Locate and identify every blood parasite.
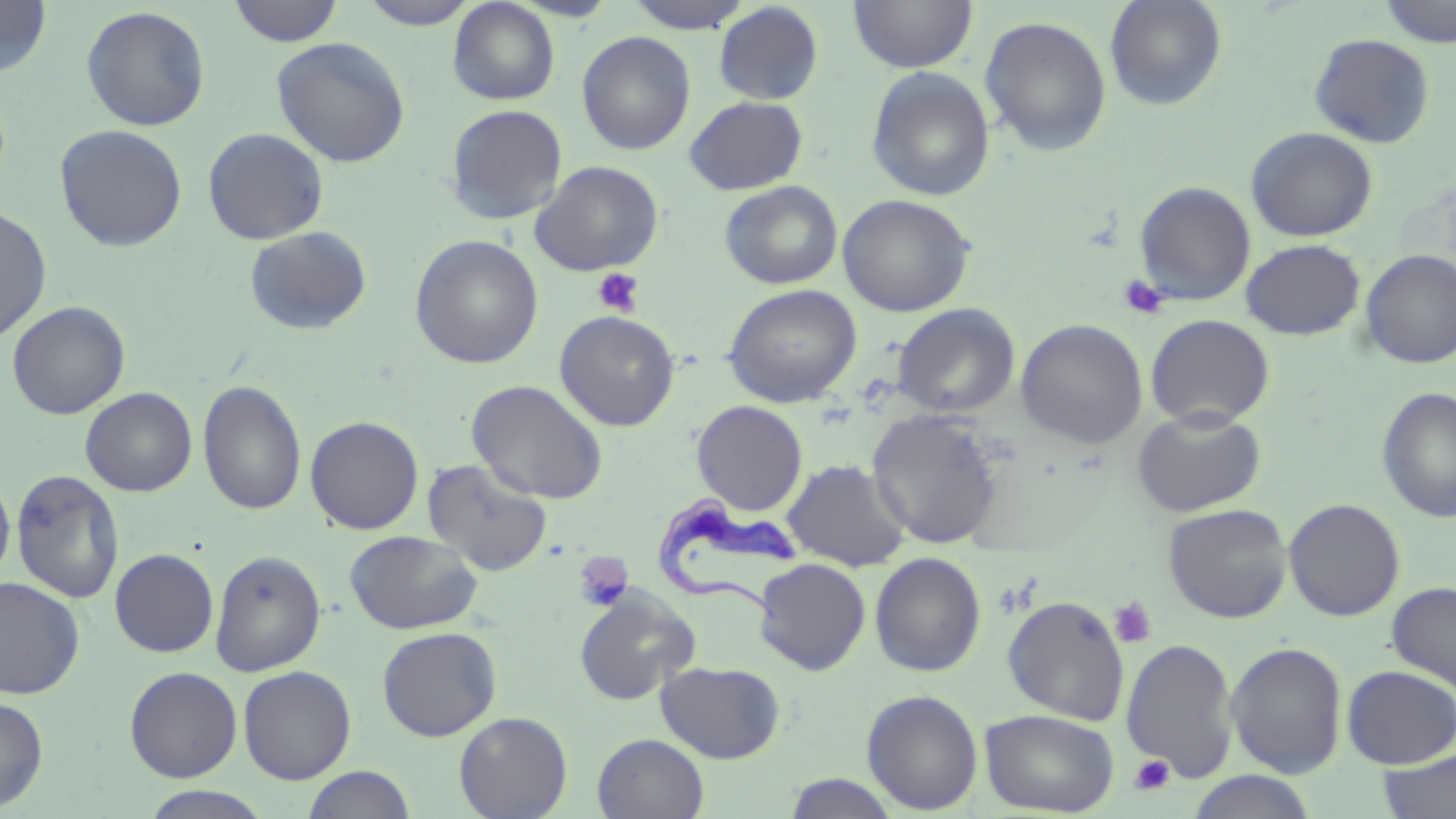
Approximate bounding boxes as (x1, y1, x2, y2) in pixels.
Trypanosoma brucei: (658, 495, 804, 625).
No Plasmodium falciparum, Plasmodium ovale, Plasmodium malariae, Plasmodium vivax, or Babesia divergens observed.

Platelet locations: (591, 267, 645, 317), (1119, 275, 1170, 320), (573, 551, 632, 612), (1109, 597, 1157, 649), (1129, 754, 1175, 796). Uninfected red blood cell locations: (0, 0, 53, 78), (228, 0, 345, 47), (356, 0, 482, 29), (623, 0, 755, 33), (848, 0, 978, 74), (1105, 0, 1228, 111), (1380, 0, 1456, 47), (448, 1, 560, 105), (714, 2, 824, 105), (80, 5, 211, 131), (979, 15, 1113, 156), (576, 31, 696, 155), (1309, 33, 1435, 148), (271, 37, 411, 168), (866, 66, 995, 202), (684, 96, 808, 195), (445, 104, 568, 225), (54, 124, 188, 252), (1245, 126, 1378, 242), (202, 127, 329, 245), (530, 160, 664, 276), (720, 180, 843, 289), (1134, 181, 1256, 305), (837, 194, 976, 317), (0, 205, 52, 345), (244, 226, 372, 336), (409, 234, 544, 369), (1241, 239, 1366, 341), (1359, 249, 1456, 369), (723, 284, 862, 407), (7, 300, 130, 420), (892, 303, 1020, 418), (554, 310, 680, 431), (1145, 314, 1275, 429), (1016, 319, 1148, 449), (198, 379, 307, 516), (467, 379, 609, 505), (81, 386, 197, 497), (1376, 386, 1456, 523), (691, 400, 808, 515), (1132, 408, 1266, 518), (305, 415, 424, 535), (422, 458, 553, 578), (782, 458, 911, 572), (10, 468, 124, 604), (0, 469, 15, 589), (872, 479, 1012, 620), (1283, 498, 1405, 621), (1163, 503, 1293, 624), (344, 530, 482, 635), (110, 549, 218, 657), (210, 549, 326, 676), (869, 552, 986, 676), (754, 558, 871, 674), (0, 577, 85, 700), (1386, 581, 1456, 694), (574, 588, 700, 705), (1002, 595, 1130, 725), (377, 626, 502, 741), (1120, 637, 1239, 782), (1226, 640, 1347, 778), (656, 661, 785, 763), (238, 665, 356, 784), (1341, 665, 1456, 768), (124, 666, 243, 782), (861, 688, 984, 814), (0, 696, 49, 811), (980, 708, 1119, 817), (454, 711, 573, 819), (592, 733, 710, 818), (1378, 749, 1456, 819), (301, 765, 417, 819), (1186, 770, 1317, 818), (782, 772, 900, 818), (139, 786, 273, 819). Slide-level diagnosis: Trypanosoma brucei. Optical microscopy. 1000x magnification. One field of a larger specimen. Thin blood film. May-Grünwald-Giemsa stain. Image is 1456×819 pixels.